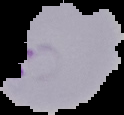

Image is 124×115 pixels. Segmented cell region on a black background. Malaria status: parasitized. From a thin blood smear.